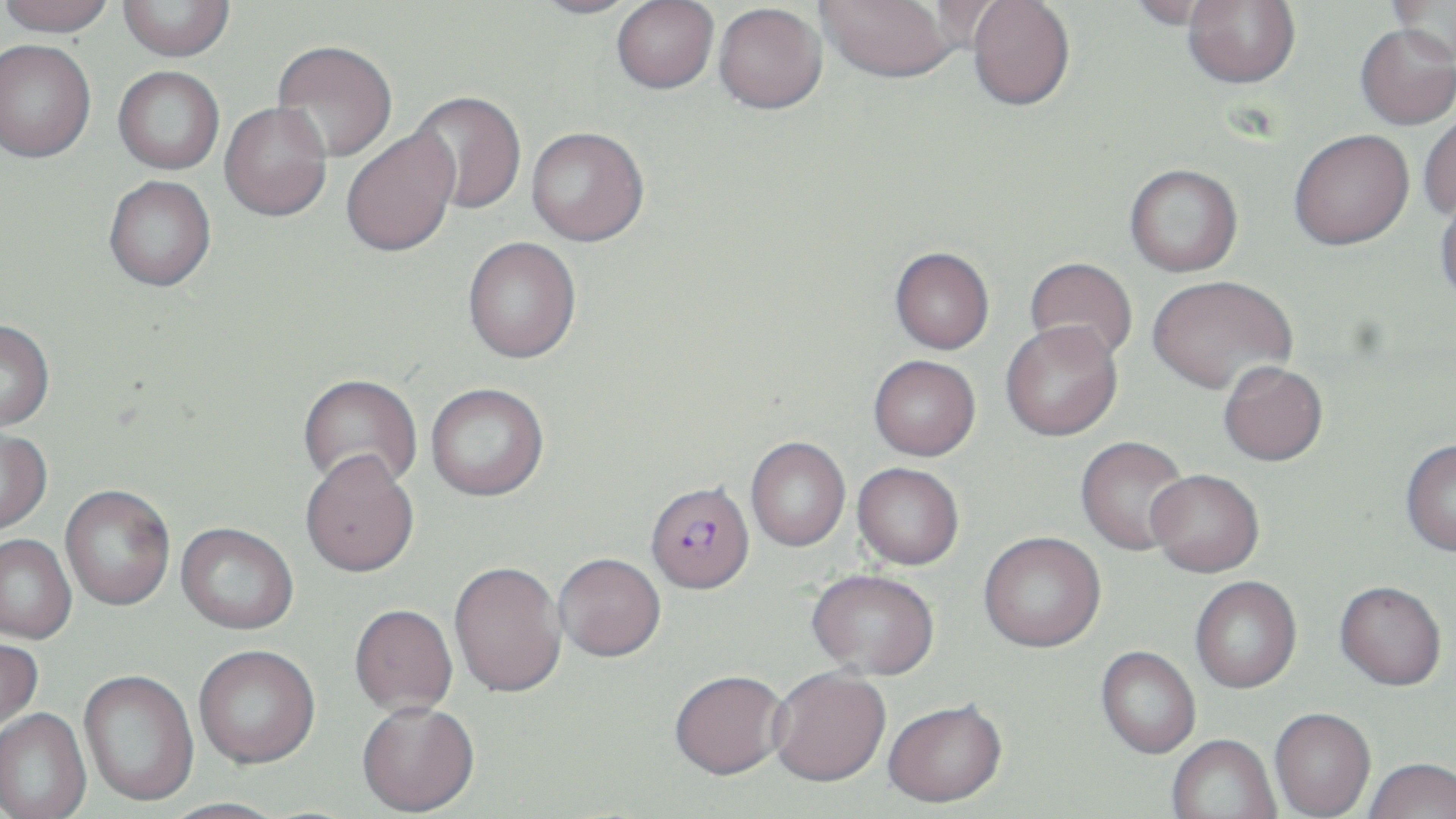
Summary:
  - Coordinate format: approximate bounding boxes as (x1,y1)-(x2,y2) corner pairs in pixels
  - Uninfected red blood cell locations: (0,0)-(115,37), (118,0)-(234,61), (529,0)-(645,18), (612,0)-(719,93), (967,0)-(1075,111), (1126,0)-(1236,29), (817,1)-(959,82), (925,1)-(1020,53), (1183,1)-(1301,88), (1386,1)-(1455,62), (713,3)-(827,114), (1355,23)-(1456,129), (0,39)-(96,163), (272,40)-(397,162), (113,66)-(224,174), (407,91)-(526,216), (220,102)-(332,221), (1417,108)-(1456,220), (526,126)-(649,245), (341,129)-(459,258), (1289,129)-(1414,250), (1124,164)-(1243,277), (104,176)-(216,291), (1435,193)-(1456,307), (462,237)-(581,363), (889,249)-(994,356), (1024,259)-(1137,366), (1147,278)-(1297,398), (0,320)-(54,430), (1000,325)-(1122,443), (868,358)-(980,464), (1218,365)-(1328,470), (298,374)-(422,492), (425,383)-(549,501), (0,427)-(51,534), (746,439)-(850,553), (1076,439)-(1191,556), (1400,441)-(1456,560), (299,451)-(419,577), (852,465)-(963,572), (1147,473)-(1264,581), (60,485)-(175,610), (176,522)-(298,633), (0,534)-(76,643), (979,535)-(1107,656), (554,555)-(666,664), (449,561)-(566,698), (806,573)-(939,683), (1190,578)-(1302,696), (1334,584)-(1446,694), (349,604)-(458,717), (0,637)-(43,738), (194,645)-(320,768), (1096,648)-(1200,760), (79,670)-(198,807), (769,671)-(891,791), (669,674)-(789,784), (357,702)-(480,817), (883,703)-(1008,811), (0,709)-(91,819), (1270,710)-(1375,818), (1167,737)-(1281,819), (1365,761)-(1456,819), (161,797)-(289,819)
  - Plasmodium falciparum-infected red blood cell locations: (645,485)-(755,598)
  - Slide-level diagnosis: Plasmodium falciparum
  - Preparation: thin blood film
  - Image size: 1456×819 pixels
  - Field of view: one of a larger specimen
  - Magnification: 1000x
  - Modality: light microscopy
  - Stain: May-Grünwald-Giemsa